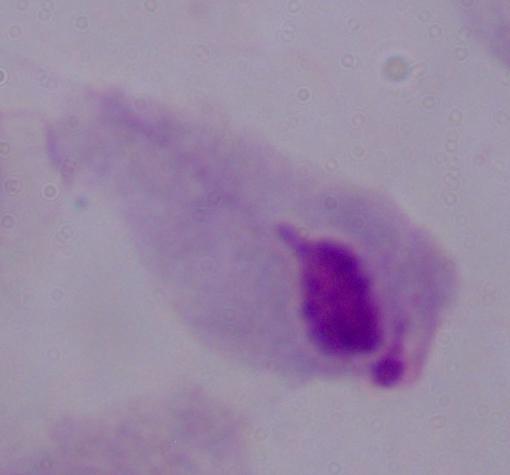 Photomicrograph. A trichomonad is seen. 1000x magnification.